Locate every Plasmodium ovale-infected red blood cell.
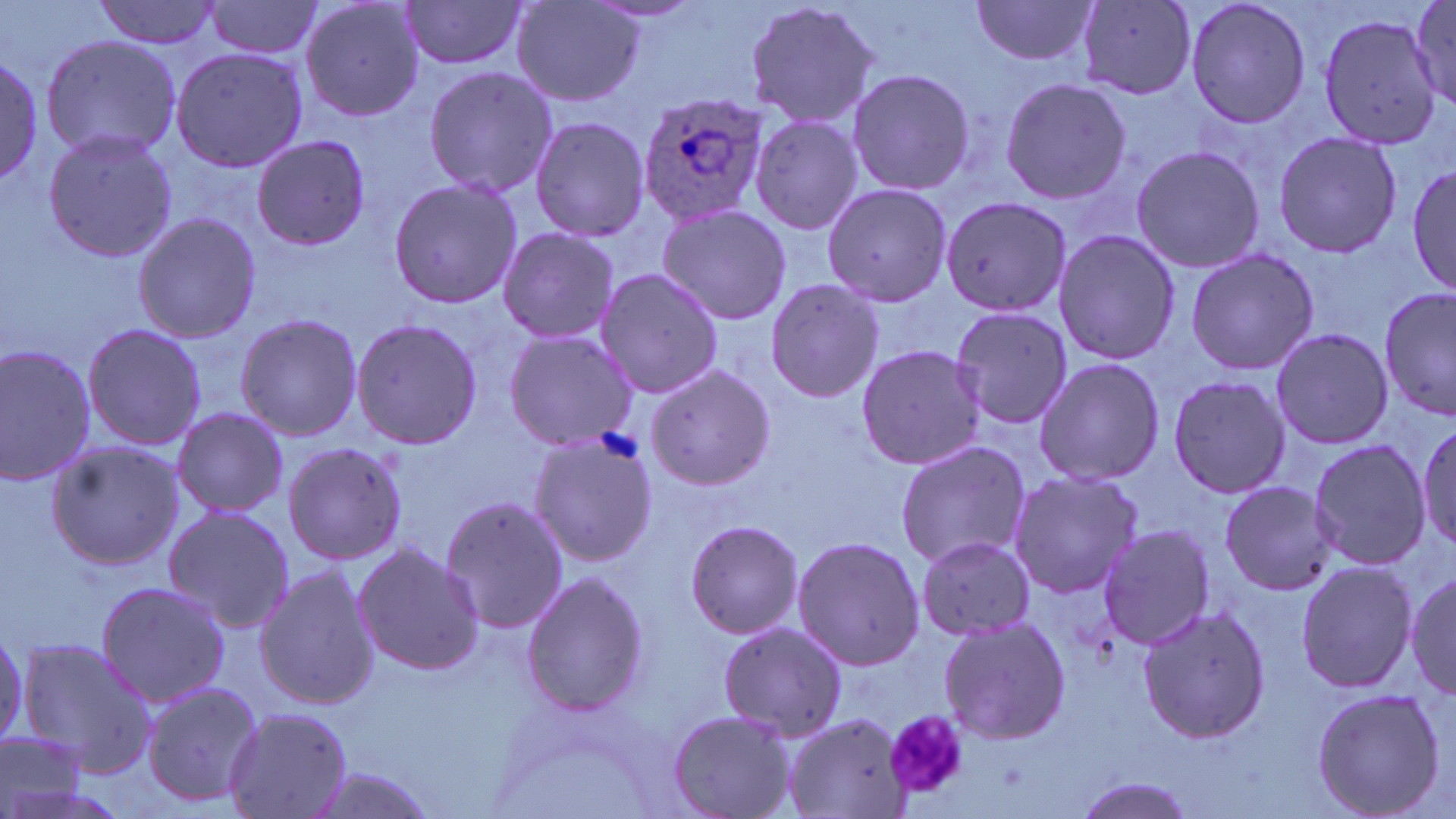

Approximate bounding boxes as (x1,y1)-(x2,y2) corner pairs in pixels.
Plasmodium ovale-infected red blood cells: (635,93)-(766,228).

Platelet locations: (883,707)-(970,799). Uninfected red blood cell locations: (298,0)-(426,121), (399,0)-(530,72), (743,0)-(884,135), (969,0)-(1099,66), (1182,0)-(1314,130), (94,1)-(223,50), (203,1)-(327,59), (511,1)-(644,108), (1407,1)-(1456,110), (1076,2)-(1196,98), (1315,11)-(1442,150), (40,34)-(184,161), (169,46)-(308,173), (0,50)-(44,187), (423,64)-(557,200), (845,67)-(976,196), (997,77)-(1132,206), (749,113)-(864,238), (528,114)-(651,244), (40,127)-(179,264), (1272,129)-(1403,261), (251,134)-(370,250), (1129,143)-(1265,274), (1410,163)-(1456,296), (388,177)-(521,310), (820,182)-(951,305), (940,194)-(1070,319), (656,204)-(792,327), (133,211)-(263,343), (495,227)-(621,347), (1052,229)-(1180,365), (1185,246)-(1319,377), (594,267)-(726,396), (764,279)-(883,402), (1377,287)-(1456,419), (947,305)-(1073,429), (234,312)-(364,442), (350,316)-(482,451), (82,321)-(206,453), (1269,324)-(1393,451), (502,330)-(640,452), (0,343)-(98,487), (855,344)-(987,471), (1032,356)-(1166,487), (645,362)-(774,493), (1166,373)-(1290,500), (170,406)-(289,517), (1415,420)-(1454,554), (527,431)-(660,569), (1307,437)-(1431,574), (47,439)-(187,571), (895,439)-(1031,570), (282,440)-(408,566), (1006,468)-(1142,601), (1215,482)-(1338,596), (440,493)-(569,634), (162,505)-(296,633), (683,519)-(807,639), (1094,524)-(1215,648), (790,534)-(925,672), (915,536)-(1038,638), (351,542)-(485,676), (1294,560)-(1417,694), (254,565)-(378,712), (1405,569)-(1456,702), (520,570)-(650,718), (95,579)-(230,709), (1134,604)-(1272,745), (936,614)-(1071,747), (718,617)-(849,743), (0,632)-(27,747), (16,637)-(157,776), (140,679)-(264,810), (1309,685)-(1446,819), (222,705)-(353,819), (667,709)-(797,819), (784,713)-(914,819), (0,728)-(96,819), (305,766)-(442,819), (1068,775)-(1203,818). Slide-level diagnosis: Plasmodium ovale. Thin blood smear. One field of a larger specimen. Light microscopy. May-Grünwald-Giemsa stain. 1000x magnification. Image is 1456×819 pixels.